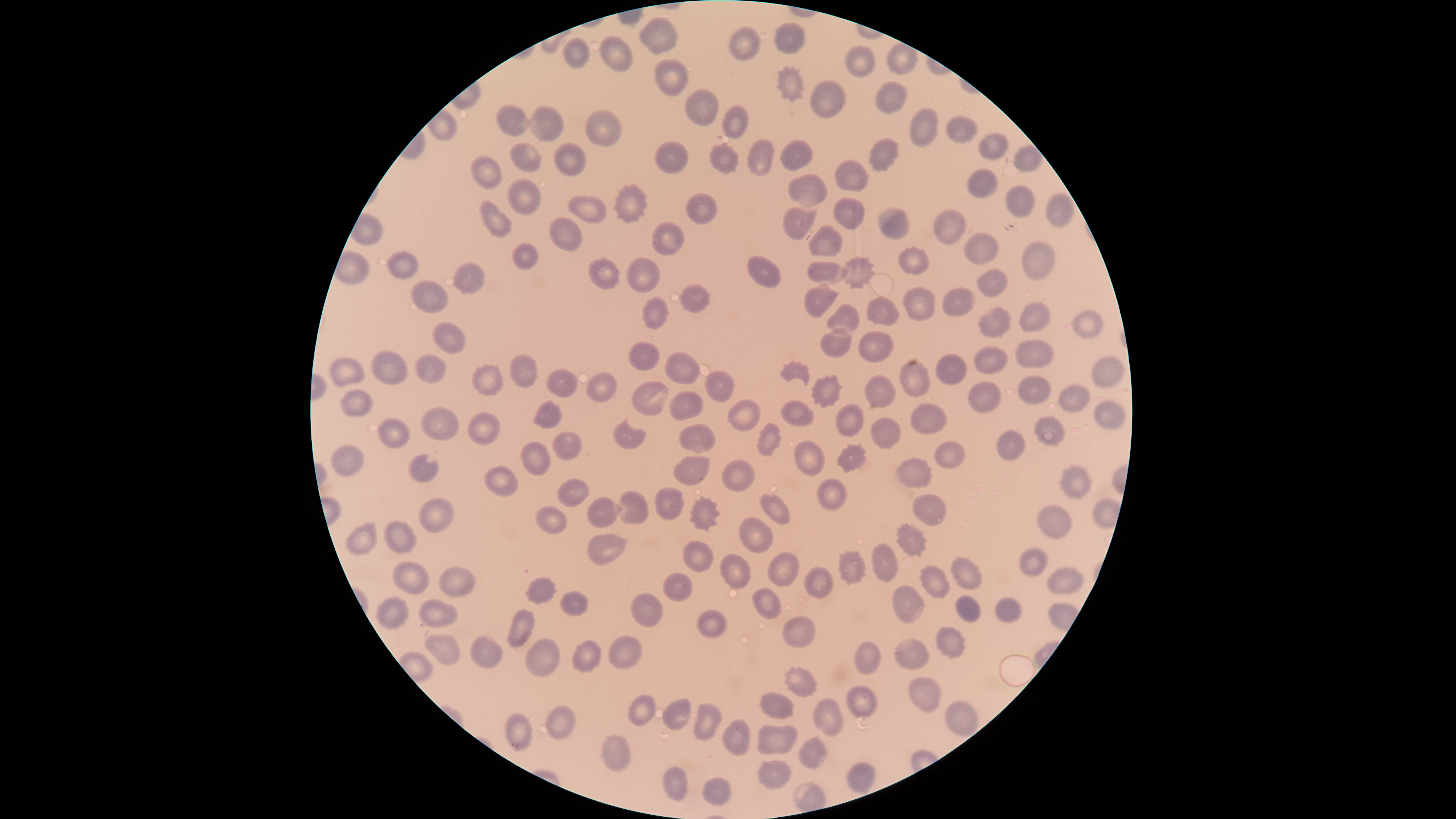
{
  "presence": "no malaria parasites identified",
  "preparation": "thin blood film",
  "field_of_view": "single",
  "capture": "smartphone photograph through the microscope eyepiece",
  "uninfected_red_blood_cells": "approximate bounding boxes as [left, top, right, bottom] in pixels: [637, 16, 678, 56], [774, 22, 806, 54], [728, 25, 760, 62], [600, 34, 635, 71], [562, 36, 590, 68], [886, 42, 919, 76], [844, 44, 877, 78], [654, 58, 690, 96], [776, 65, 808, 104], [809, 80, 847, 119], [875, 81, 908, 115], [684, 88, 719, 125], [527, 103, 566, 142], [496, 104, 533, 137], [721, 105, 750, 138], [908, 106, 939, 148], [584, 109, 622, 147], [945, 115, 978, 144], [978, 133, 1009, 162], [746, 138, 774, 177], [779, 138, 814, 172], [867, 138, 900, 172], [653, 140, 688, 174], [509, 141, 541, 173], [553, 142, 587, 177], [1013, 142, 1042, 172], [709, 143, 740, 175], [468, 155, 503, 189], [834, 159, 870, 193], [966, 166, 1000, 199], [787, 173, 829, 209], [507, 178, 542, 217], [612, 182, 650, 225], [1005, 184, 1036, 218], [686, 191, 718, 225], [1046, 192, 1074, 228], [567, 194, 607, 225], [832, 197, 864, 230], [479, 199, 513, 239], [782, 206, 818, 240], [876, 206, 909, 239], [932, 208, 967, 245], [549, 216, 583, 252], [652, 221, 685, 256], [808, 225, 843, 257], [963, 233, 999, 265], [1021, 241, 1056, 280], [510, 242, 540, 271], [896, 245, 930, 275], [385, 249, 420, 279], [587, 255, 621, 291], [840, 255, 875, 289], [625, 256, 661, 294], [746, 256, 781, 289], [806, 260, 849, 286], [451, 261, 487, 294], [977, 268, 1008, 298], [411, 279, 447, 314], [804, 282, 840, 317], [678, 283, 711, 314], [902, 286, 937, 322], [942, 288, 976, 316], [866, 296, 900, 327], [641, 297, 669, 330], [1018, 302, 1051, 333], [825, 303, 861, 336], [978, 306, 1012, 339], [1073, 310, 1103, 340], [432, 322, 465, 354], [820, 326, 852, 357], [858, 331, 893, 363], [1015, 339, 1054, 369], [627, 341, 660, 371], [973, 346, 1008, 373], [370, 350, 408, 385], [664, 351, 700, 386], [414, 353, 447, 383], [508, 353, 539, 389], [936, 353, 968, 385], [1091, 354, 1126, 389], [328, 356, 365, 388], [898, 359, 931, 398], [779, 360, 811, 386], [471, 363, 505, 396], [546, 368, 578, 398], [704, 369, 735, 404], [586, 371, 617, 403], [811, 373, 844, 408], [865, 375, 896, 408], [1017, 376, 1052, 405], [630, 381, 670, 416], [967, 381, 1001, 413], [1057, 383, 1090, 414], [340, 389, 375, 417], [668, 390, 705, 420], [726, 398, 762, 432], [532, 399, 563, 429], [780, 399, 814, 426], [1092, 399, 1129, 430], [835, 402, 864, 438], [910, 402, 948, 435], [421, 405, 458, 441], [468, 411, 501, 444], [870, 416, 902, 449], [1033, 416, 1066, 447], [613, 418, 647, 450], [378, 419, 410, 450], [755, 421, 782, 457], [679, 423, 716, 455], [552, 429, 583, 461], [997, 430, 1027, 462], [933, 439, 966, 469], [793, 440, 825, 477], [520, 441, 552, 477], [836, 443, 867, 474], [330, 444, 363, 477], [408, 452, 438, 484], [673, 455, 711, 486], [895, 456, 932, 489], [721, 458, 756, 493], [1057, 463, 1095, 499], [484, 466, 519, 498], [556, 477, 589, 508], [816, 477, 847, 510], [654, 485, 685, 521], [617, 490, 649, 525], [759, 494, 791, 526], [912, 494, 947, 526], [586, 495, 623, 528], [688, 495, 721, 531], [418, 497, 454, 533], [534, 504, 567, 535], [1037, 505, 1073, 539], [738, 516, 775, 553], [382, 519, 417, 554], [344, 522, 377, 555], [895, 522, 929, 558], [587, 532, 628, 567], [682, 541, 715, 573], [871, 542, 899, 583], [1019, 547, 1048, 574], [838, 549, 867, 585], [767, 552, 800, 588], [719, 553, 752, 591], [949, 556, 984, 590], [392, 561, 430, 595], [439, 565, 475, 599], [804, 565, 834, 599], [919, 566, 951, 599], [1047, 566, 1086, 594], [662, 572, 694, 602], [524, 576, 558, 606], [892, 584, 926, 624], [751, 587, 783, 620], [559, 591, 588, 616], [631, 592, 664, 628], [954, 594, 981, 622], [374, 595, 409, 630], [993, 596, 1022, 624], [418, 598, 459, 628], [505, 609, 535, 648], [696, 609, 726, 640], [782, 615, 817, 648], [934, 626, 967, 660], [424, 633, 461, 665], [607, 634, 643, 670], [470, 635, 504, 669], [894, 637, 930, 670], [524, 638, 561, 678], [571, 640, 602, 674], [854, 641, 881, 676], [908, 677, 941, 713], [846, 685, 878, 719], [758, 691, 796, 721], [628, 694, 657, 727], [813, 697, 844, 737], [663, 698, 692, 731], [944, 700, 979, 739], [693, 702, 724, 741], [545, 704, 576, 741], [503, 713, 534, 751], [721, 719, 751, 756], [756, 724, 799, 757], [602, 734, 631, 772], [798, 734, 827, 770], [757, 760, 792, 791], [846, 761, 877, 794], [662, 766, 688, 801], [702, 777, 732, 807]",
  "stain": "Giemsa",
  "image_size": "1456×819 pixels",
  "visible_region": "circular"
}